Point out each leukocyte.
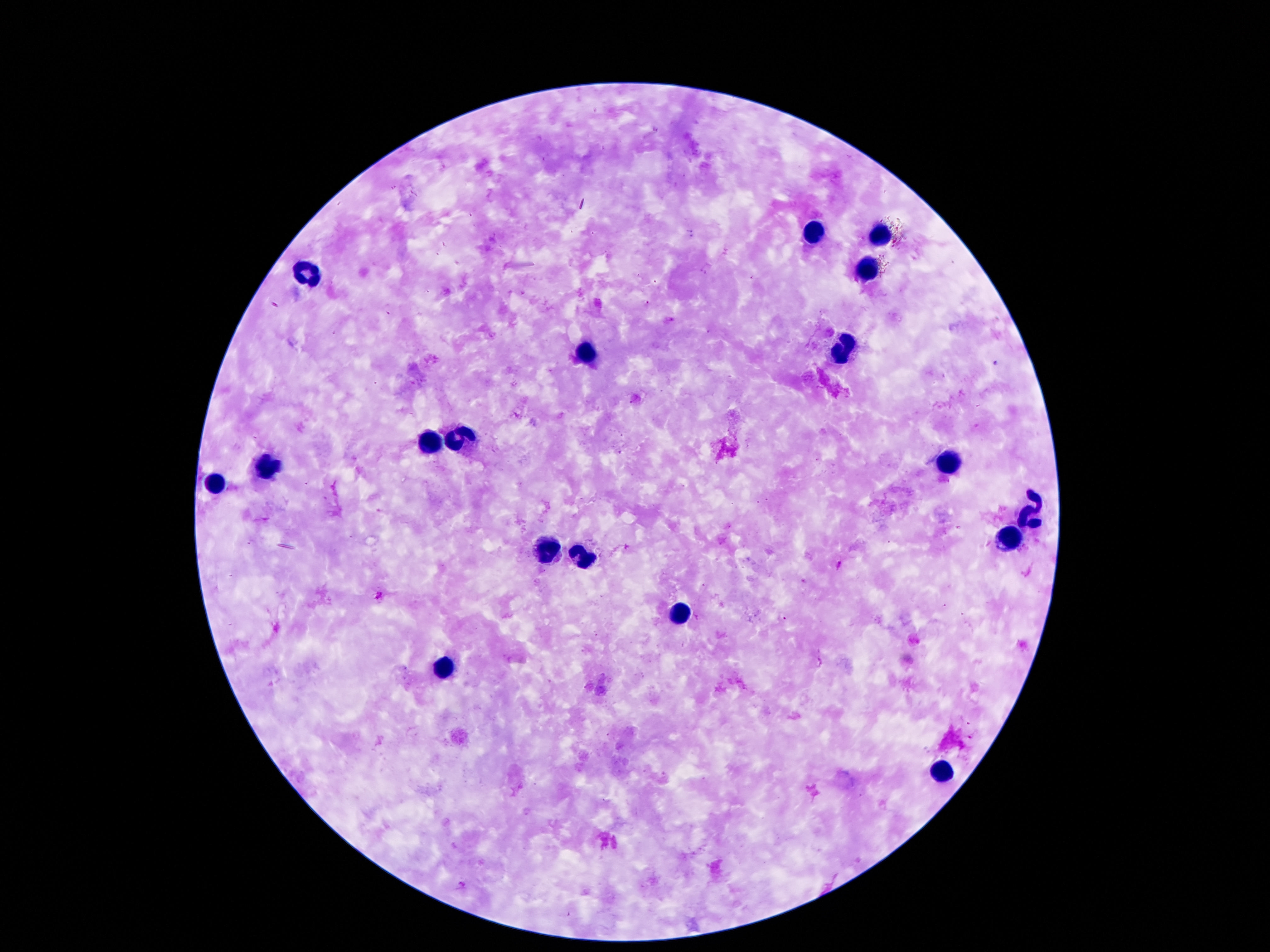

Approximate object centers, in pixels from the top-left corner.
Leukocytes: (x=809, y=234), (x=882, y=234), (x=870, y=266), (x=303, y=271), (x=843, y=350), (x=589, y=352), (x=462, y=439), (x=425, y=442), (x=948, y=460), (x=266, y=468), (x=216, y=485), (x=1034, y=511), (x=1011, y=534), (x=548, y=551), (x=585, y=558), (x=680, y=612), (x=444, y=669), (x=942, y=771).

magnification = 100x
patient malaria status = uninfected
capture = smartphone camera through the microscope eyepiece
stain = Giemsa
preparation = thick blood smear
image size = 1270×952 pixels
field of view = single